Give the position of every malaria parasite.
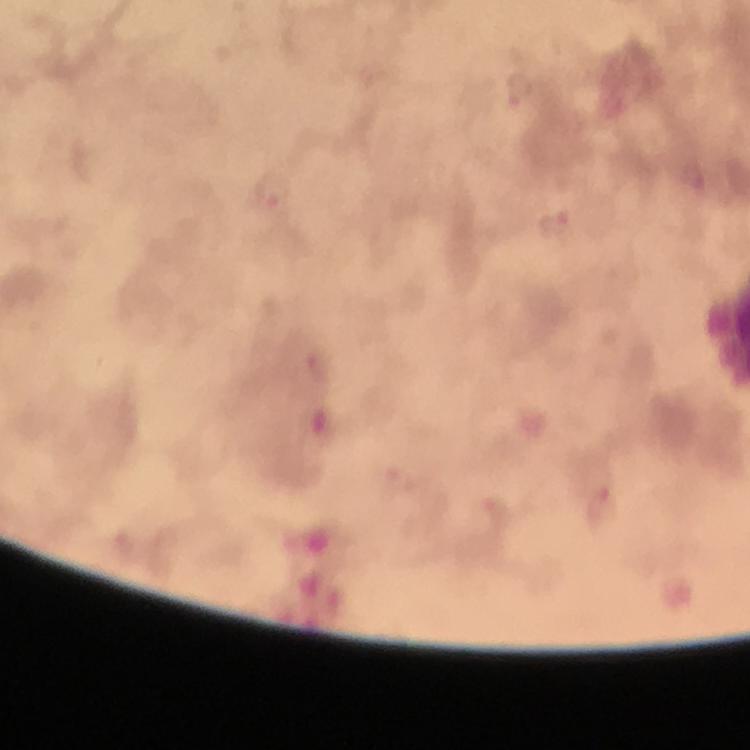
Approximate object centers, in pixels from the top-left corner.
Malaria parasites: (x=521, y=92), (x=273, y=192), (x=556, y=227), (x=602, y=504).

Image is 750×750 pixels. Giemsa-stained preparation. Immersion oil applied. At 100x magnification. Thick blood smear. Photographed through the microscope with a smartphone camera. From a malaria diagnostic workup. A crop from one field of view.